Report the malaria status of this cell.
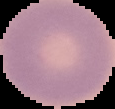
Uninfected.

Cell region segmented out of the field of view; the surrounding area is masked to black. Image is 115×109 pixels. From a thin blood smear.